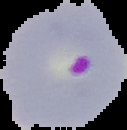

image size = 127×130 pixels
malaria status = parasitized
image type = segmented cell region with the area outside set to black
preparation = thin blood film